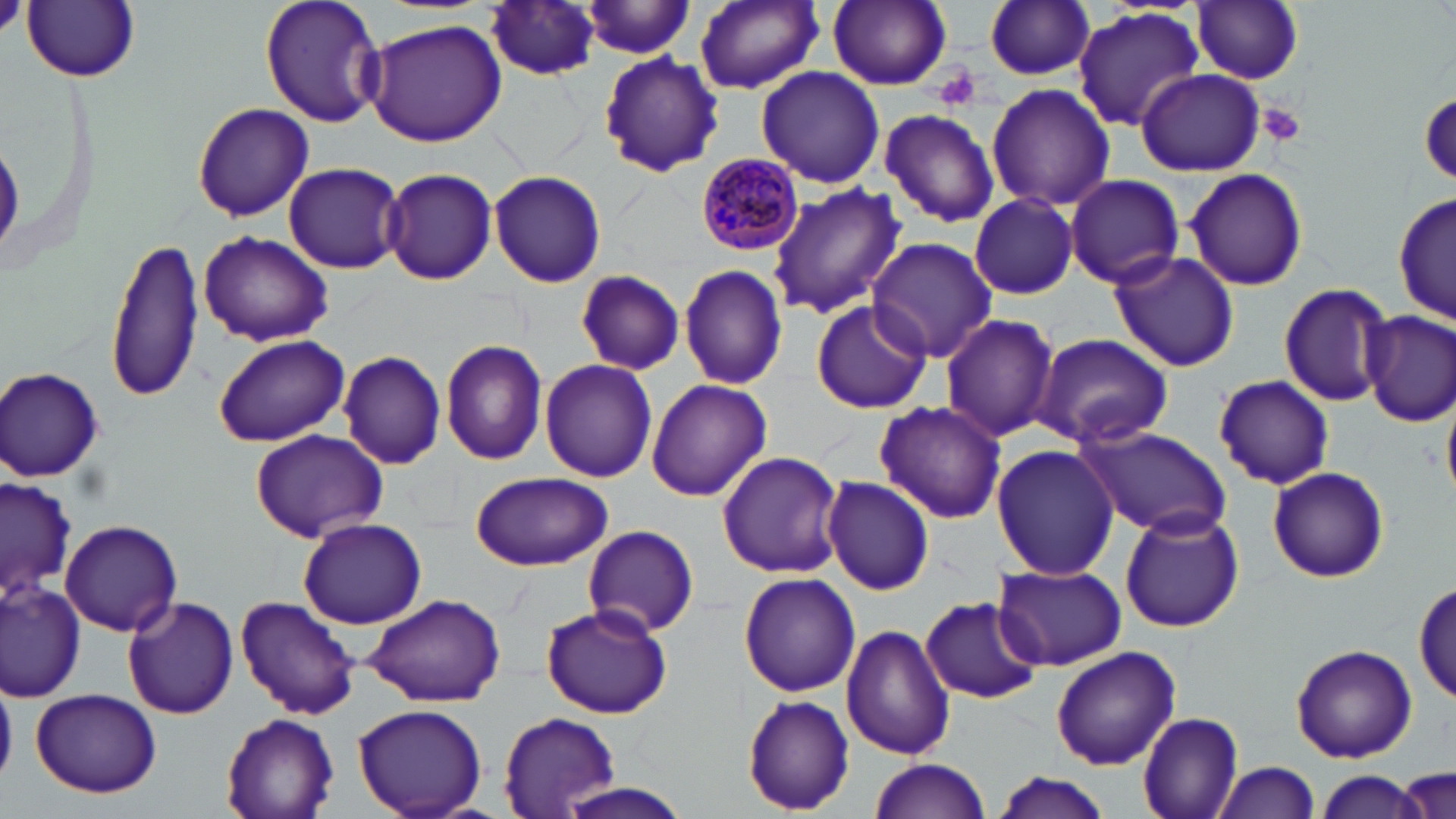 Approximate bounding boxes as [x1, y1, x2, y2] in pixels. Plasmodium malariae-infected red blood cell locations: [692, 150, 808, 256]. Uninfected red blood cell locations: [23, 0, 141, 83], [260, 0, 386, 128], [694, 0, 823, 94], [828, 0, 953, 90], [1190, 0, 1304, 84], [483, 1, 600, 81], [986, 1, 1096, 81], [577, 2, 697, 59], [1073, 8, 1206, 131], [360, 18, 506, 147], [598, 51, 725, 176], [755, 66, 884, 189], [1137, 69, 1263, 175], [985, 83, 1114, 213], [1419, 92, 1456, 185], [190, 102, 314, 223], [879, 107, 1000, 228], [283, 161, 405, 274], [381, 169, 498, 285], [486, 169, 609, 286], [1184, 169, 1309, 291], [1063, 173, 1185, 289], [768, 182, 906, 321], [1395, 191, 1455, 330], [970, 193, 1079, 300], [198, 230, 332, 348], [104, 236, 210, 405], [866, 237, 997, 363], [1107, 248, 1240, 372], [679, 263, 790, 391], [574, 269, 685, 375], [1278, 283, 1390, 407], [810, 298, 933, 416], [1361, 310, 1456, 426], [939, 313, 1060, 443], [211, 333, 350, 446], [1032, 333, 1172, 449], [442, 339, 548, 468], [338, 351, 445, 470], [539, 358, 657, 482], [0, 365, 107, 483], [1215, 374, 1335, 490], [645, 379, 772, 502], [873, 399, 1007, 524], [1075, 423, 1233, 541], [249, 428, 389, 542], [991, 444, 1119, 580], [716, 451, 845, 578], [1267, 467, 1390, 583], [469, 470, 612, 571], [1, 475, 76, 607], [820, 476, 936, 596], [1120, 508, 1244, 632], [298, 517, 427, 629], [60, 520, 183, 637], [581, 526, 699, 639], [992, 562, 1127, 671], [738, 571, 860, 696], [1415, 577, 1454, 708], [2, 580, 87, 702], [362, 593, 507, 708], [121, 596, 240, 720], [235, 596, 361, 721], [920, 596, 1042, 705], [541, 605, 672, 719], [842, 623, 956, 761], [1289, 642, 1418, 763], [1050, 646, 1181, 770], [30, 688, 162, 798], [743, 694, 855, 815], [354, 704, 486, 818], [497, 711, 617, 815], [1138, 711, 1245, 818], [221, 712, 339, 819], [869, 757, 991, 818], [1215, 760, 1320, 818], [1399, 767, 1453, 817], [1311, 772, 1431, 817], [992, 773, 1114, 819], [553, 781, 700, 819]. Platelet locations: [0, 0, 27, 40], [933, 68, 980, 110], [1257, 103, 1308, 146]. Slide-level diagnosis: Plasmodium malariae. Image is 1456×819 pixels. Optical microscopy. May-Grünwald-Giemsa stain. Thin blood smear. One field of a larger specimen. 1000x magnification.